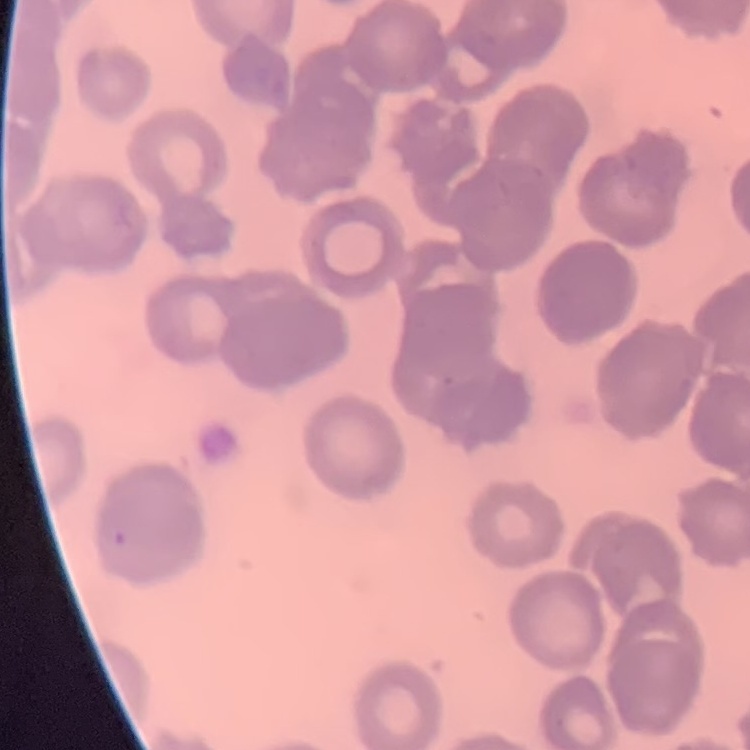
The red blood cells show rouleaux formation. One tile cut from a larger photomicrograph. Thin blood smear. Stained with either Field's or Giemsa.